Comment on the morphology of the erythrocytes.
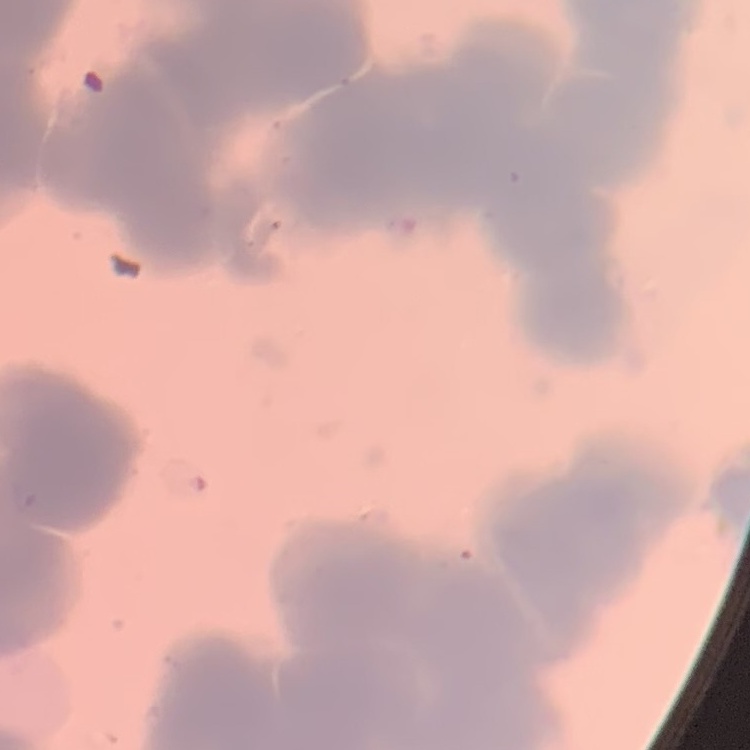

Rouleaux formation.

Thin peripheral smear. Field's or Giemsa stain. One tile cut from a larger photomicrograph.